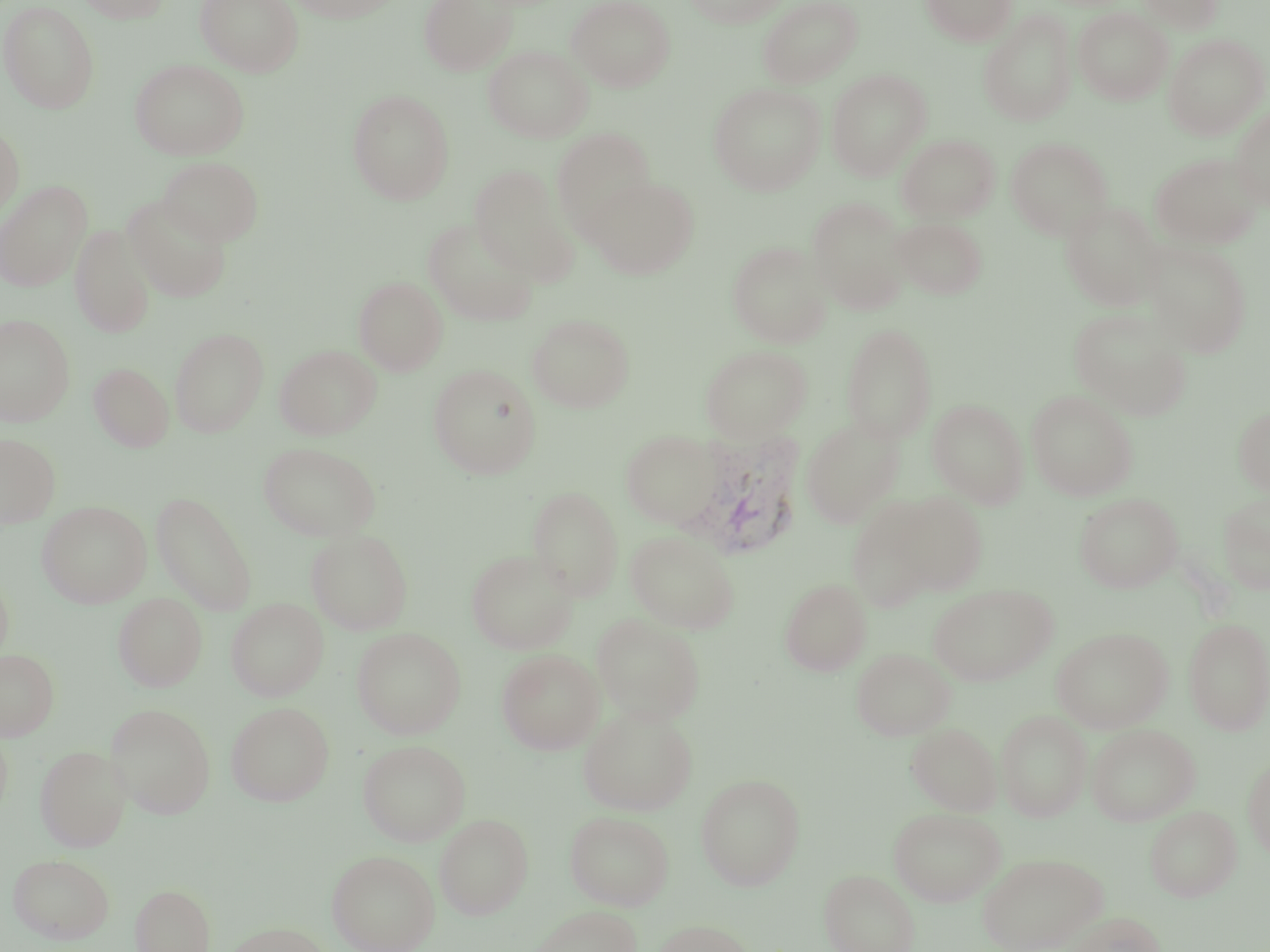
Summary:
  - Coordinate format: approximate bounding boxes as [x1, y1, x2, y2] in pixels
  - Uninfected red blood cell locations: [73, 0, 172, 23], [195, 0, 303, 76], [285, 0, 400, 22], [418, 0, 518, 76], [566, 0, 675, 92], [682, 0, 791, 28], [757, 0, 863, 88], [920, 0, 1017, 46], [1137, 0, 1225, 32], [0, 1, 100, 114], [1073, 7, 1172, 105], [979, 10, 1077, 127], [1163, 33, 1268, 140], [484, 45, 592, 142], [130, 58, 249, 160], [826, 69, 932, 181], [708, 82, 825, 195], [347, 89, 456, 205], [1231, 106, 1270, 211], [0, 124, 24, 222], [552, 127, 656, 239], [897, 133, 1000, 223], [1006, 137, 1113, 240], [1150, 152, 1264, 249], [158, 156, 264, 245], [469, 165, 578, 284], [587, 175, 700, 279], [1, 180, 92, 291], [123, 194, 233, 302], [807, 197, 912, 313], [1061, 201, 1165, 311], [892, 216, 988, 299], [423, 217, 540, 326], [70, 224, 156, 338], [1142, 239, 1253, 357], [727, 241, 831, 348], [354, 276, 449, 376], [1069, 307, 1192, 419], [0, 313, 76, 426], [528, 314, 634, 413], [841, 322, 938, 444], [170, 327, 268, 437], [275, 345, 381, 439], [700, 345, 811, 441], [89, 362, 174, 452], [428, 365, 542, 479], [1026, 390, 1138, 500], [927, 398, 1029, 508], [1233, 406, 1270, 496], [801, 417, 904, 527], [621, 429, 722, 529], [0, 433, 60, 528], [258, 442, 381, 541], [528, 485, 624, 600], [890, 490, 989, 596], [150, 491, 257, 615], [1218, 491, 1270, 594], [1074, 492, 1183, 592], [846, 497, 943, 613], [38, 501, 151, 608], [306, 529, 414, 635], [625, 530, 740, 633], [466, 548, 579, 654], [0, 572, 13, 668], [780, 577, 871, 676], [928, 583, 1057, 685], [113, 593, 207, 692], [226, 598, 328, 701], [592, 613, 705, 725], [1183, 617, 1270, 735], [1051, 626, 1173, 732], [351, 627, 466, 739], [851, 647, 955, 740], [0, 649, 59, 740], [497, 649, 604, 754], [226, 702, 334, 806], [106, 704, 215, 817], [578, 705, 698, 815], [997, 709, 1091, 822], [906, 722, 1002, 815], [1087, 724, 1200, 826], [358, 739, 471, 846], [36, 745, 130, 852], [1243, 759, 1270, 862], [695, 773, 806, 890], [1145, 805, 1241, 901], [888, 806, 1006, 906], [565, 810, 673, 910], [434, 813, 533, 919], [326, 849, 440, 952], [977, 851, 1107, 952], [7, 853, 115, 944], [819, 868, 920, 952], [130, 883, 215, 952], [527, 905, 642, 952], [1063, 911, 1168, 952], [651, 919, 758, 952], [223, 921, 334, 951]
  - Plasmodium vivax-infected red blood cell locations: [673, 427, 806, 559]
  - Slide-level diagnosis: Plasmodium vivax
  - Preparation: thin blood film
  - Field of view: single
  - Image size: 1270×952 pixels
  - Stain: May-Grünwald-Giemsa
  - Modality: optical microscopy
  - Magnification: 1000x